Report the malaria status of this cell.
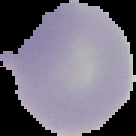

It is uninfected.

preparation = thin blood smear
image size = 136×136 pixels
image type = cell region segmented out of the field of view; surrounding area masked to black